Report the malaria status of this cell.
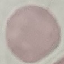

It is uninfected.

Summary:
  - Stain: Giemsa
  - Preparation: thin blood smear
  - Image type: automatically extracted cell patch, resized to 64 × 64 pixels
  - Capture: smartphone camera at the microscope eyepiece